Identify the parasite.
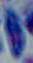

Toxoplasma gondii.

{
  "modality": "photomicrograph",
  "magnification": "1000x"
}